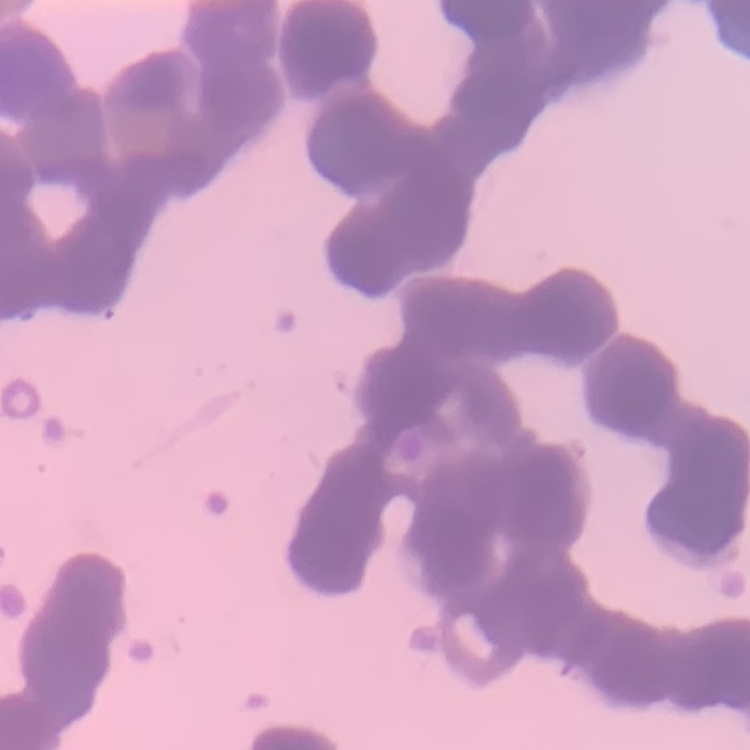
Summary:
  - Red blood cell morphology: rouleaux formation
  - Image type: square crop of a larger photomicrograph
  - Stain: Field's or Giemsa
  - Preparation: thin peripheral smear